Outline each uninfected red blood cell.
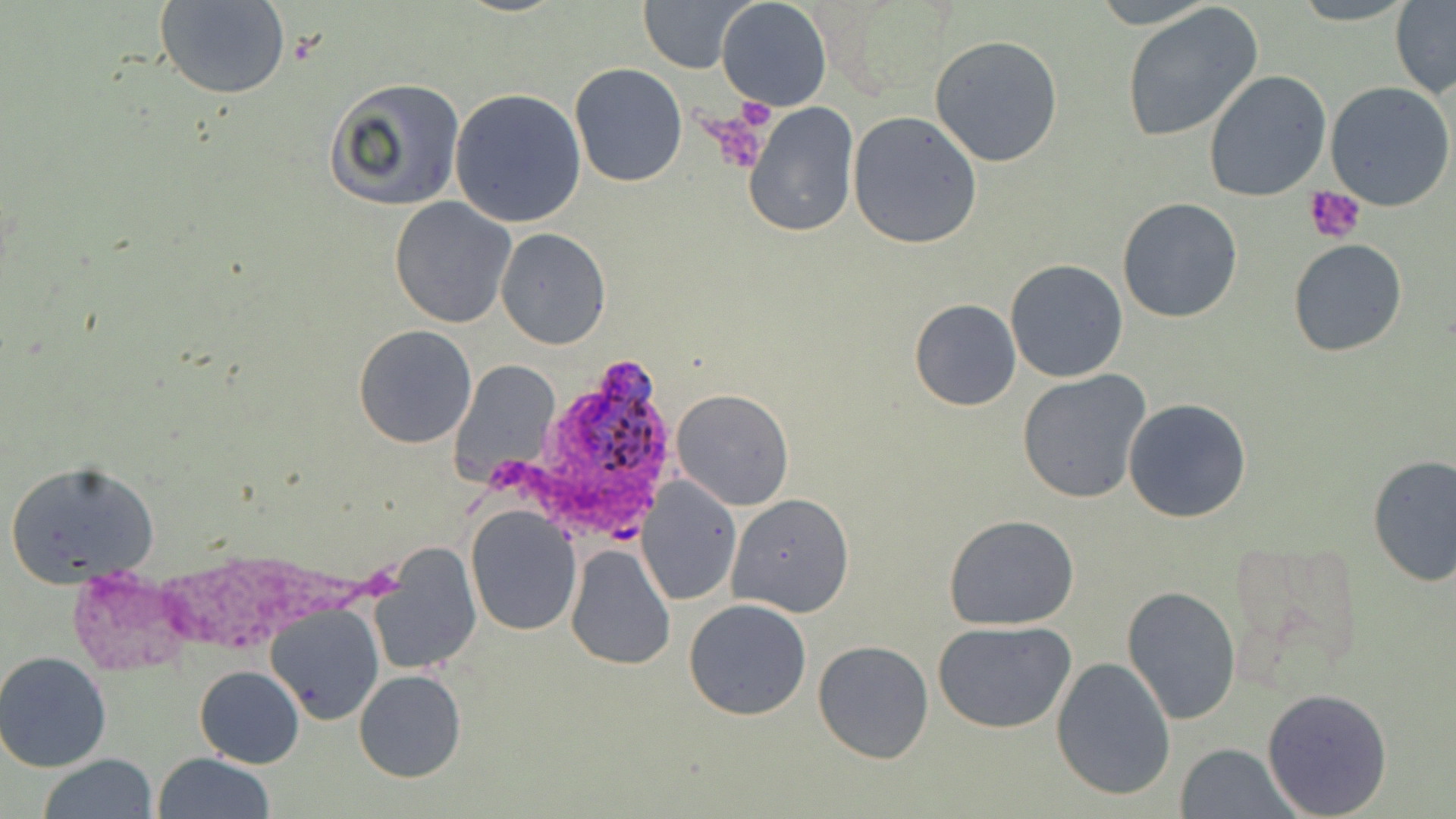

Approximate bounding boxes as (x1, y1, x2, y2) in pixels.
Uninfected red blood cells: (157, 0, 292, 100), (638, 0, 757, 74), (716, 0, 832, 112), (1287, 0, 1418, 25), (1391, 2, 1456, 97), (1120, 3, 1264, 143), (930, 34, 1063, 168), (570, 63, 687, 187), (1203, 70, 1332, 201), (324, 77, 465, 213), (1326, 82, 1454, 212), (448, 89, 588, 229), (741, 102, 860, 238), (848, 111, 982, 249), (390, 198, 515, 328), (1117, 199, 1242, 322), (495, 228, 611, 349), (1287, 238, 1408, 357), (1004, 259, 1129, 383), (909, 299, 1021, 412), (353, 324, 477, 448), (448, 358, 560, 485), (1017, 368, 1153, 504), (670, 387, 795, 511), (1123, 398, 1253, 524), (1366, 454, 1456, 590), (6, 460, 161, 588), (636, 476, 742, 606), (727, 492, 855, 616), (465, 506, 580, 634), (944, 514, 1080, 629), (1220, 535, 1364, 696), (368, 541, 483, 674), (564, 544, 676, 670), (1121, 586, 1241, 725), (684, 599, 812, 720), (267, 602, 385, 726), (932, 620, 1077, 734), (813, 641, 935, 763), (0, 651, 115, 772), (1052, 656, 1177, 801), (194, 665, 305, 767), (354, 668, 467, 783), (1262, 685, 1392, 817), (1174, 742, 1300, 819), (152, 753, 276, 818), (38, 756, 159, 818).

Platelet locations: (733, 97, 776, 134), (700, 110, 772, 171), (1304, 186, 1368, 244). Plasmodium ovale-infected red blood cell locations: (543, 357, 684, 503). Slide-level diagnosis: Plasmodium ovale. Thin blood smear. 1000x magnification. May-Grünwald-Giemsa stain. Light microscopy. Image is 1456×819 pixels. One field of a larger specimen.